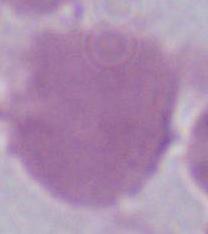
Summary:
  - Identification: erythrocyte
  - Modality: micrograph
  - Magnification: 1000x